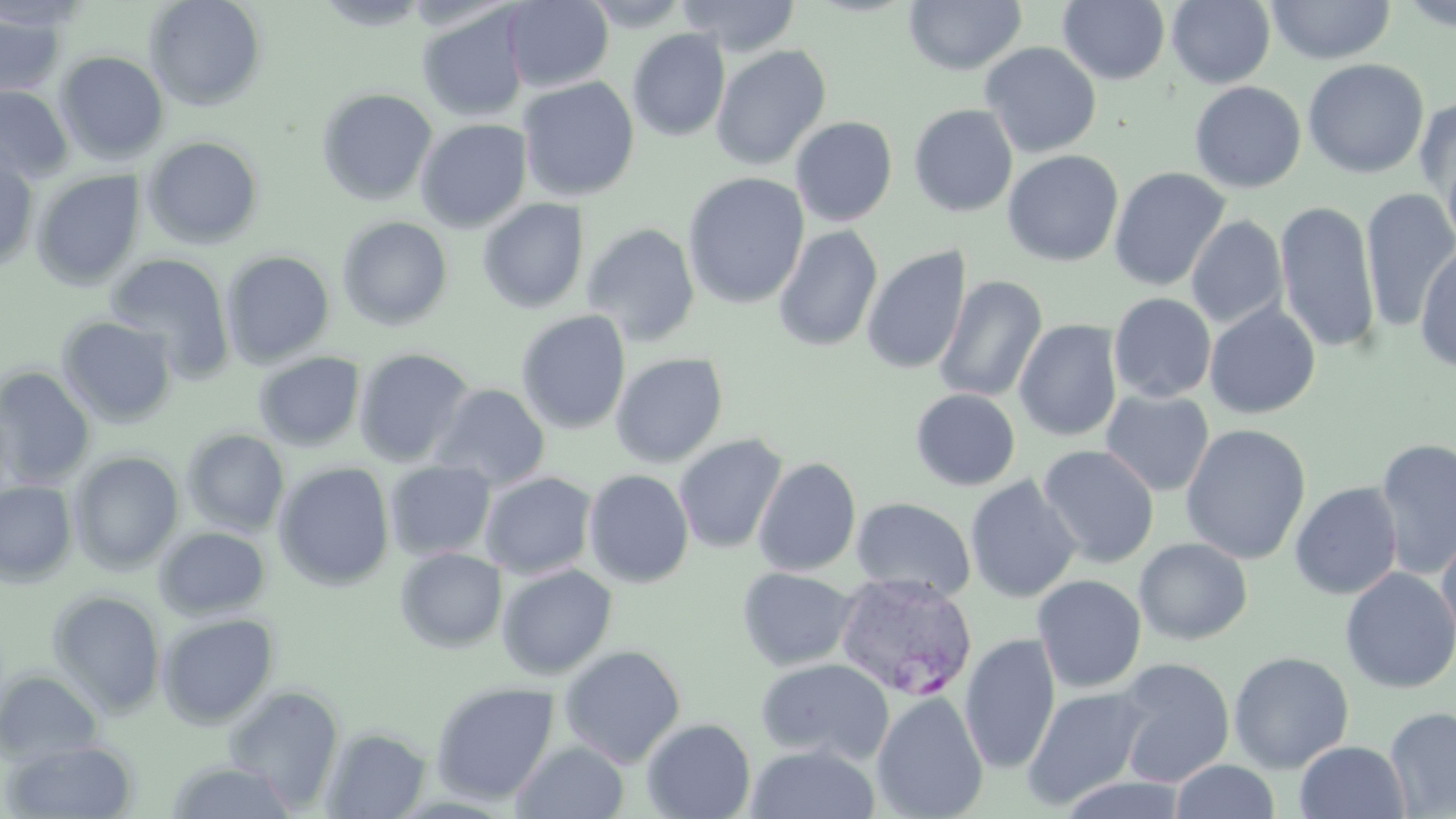
Summary:
  - Coordinate format: approximate bounding boxes as (x1,y1)-(x2,y2) corner pairs in pixels
  - Plasmodium vivax-infected red blood cell locations: (833,571)-(978,701)
  - Uninfected red blood cell locations: (143,0)-(267,111), (502,0)-(614,92), (580,0)-(691,30), (676,0)-(802,57), (1166,0)-(1275,89), (1266,0)-(1395,65), (904,1)-(1026,75), (1057,1)-(1171,85), (312,2)-(435,30), (1397,2)-(1456,33), (416,6)-(530,123), (0,8)-(69,100), (627,28)-(731,142), (980,41)-(1101,158), (710,44)-(832,170), (54,50)-(169,165), (1302,58)-(1430,178), (517,76)-(640,202), (1189,81)-(1306,193), (0,85)-(74,183), (316,87)-(438,206), (1413,94)-(1456,206), (909,104)-(1018,217), (790,113)-(1016,221), (790,116)-(897,227), (415,118)-(533,233), (141,135)-(265,250), (1441,144)-(1456,257), (0,148)-(40,272), (1002,150)-(1123,267), (1109,167)-(1230,292), (31,169)-(146,290), (682,172)-(810,309), (1361,187)-(1456,332), (477,198)-(589,314), (1275,200)-(1380,353), (336,215)-(454,331), (1186,215)-(1287,329), (581,223)-(701,347), (773,225)-(883,352), (1415,244)-(1456,372), (861,246)-(972,376), (220,249)-(335,367), (105,252)-(235,380), (934,275)-(1047,403), (1109,292)-(1216,403), (1203,301)-(1321,419), (516,310)-(631,434), (56,315)-(178,428), (1014,319)-(1123,442), (353,347)-(476,467), (252,351)-(366,451), (610,351)-(729,467), (0,367)-(96,487), (430,383)-(550,491), (910,389)-(1021,491), (1100,389)-(1215,496), (1180,423)-(1311,565), (181,428)-(290,537), (673,433)-(788,554), (1375,439)-(1456,580), (1037,444)-(1160,568), (68,450)-(184,574), (753,456)-(861,576), (384,460)-(496,561), (273,461)-(395,591), (583,468)-(694,588), (480,471)-(598,579), (964,475)-(1081,604), (0,479)-(78,586), (1289,482)-(1403,599), (850,497)-(976,602), (154,525)-(271,620), (1436,527)-(1456,648), (1134,537)-(1253,645), (395,547)-(507,653), (496,564)-(618,680), (737,566)-(858,671), (1339,567)-(1456,694), (1031,575)-(1147,693), (47,589)-(166,718), (157,613)-(280,729), (960,633)-(1060,775), (558,644)-(686,768), (1228,650)-(1354,773), (756,657)-(894,766), (1113,657)-(1235,787), (0,669)-(104,764), (430,681)-(560,804), (223,684)-(345,810), (1023,685)-(1151,812), (872,691)-(989,819), (1384,707)-(1456,818), (641,717)-(756,819), (321,726)-(432,818), (3,739)-(139,818), (512,740)-(629,818), (1294,740)-(1411,819), (745,744)-(880,819), (165,759)-(299,819), (1169,760)-(1281,819)
  - Slide-level diagnosis: Plasmodium vivax
  - Modality: optical microscopy
  - Image size: 1456×819 pixels
  - Stain: May-Grünwald-Giemsa
  - Preparation: thin blood film
  - Magnification: 1000x
  - Field of view: single